Identify the blood parasite species.
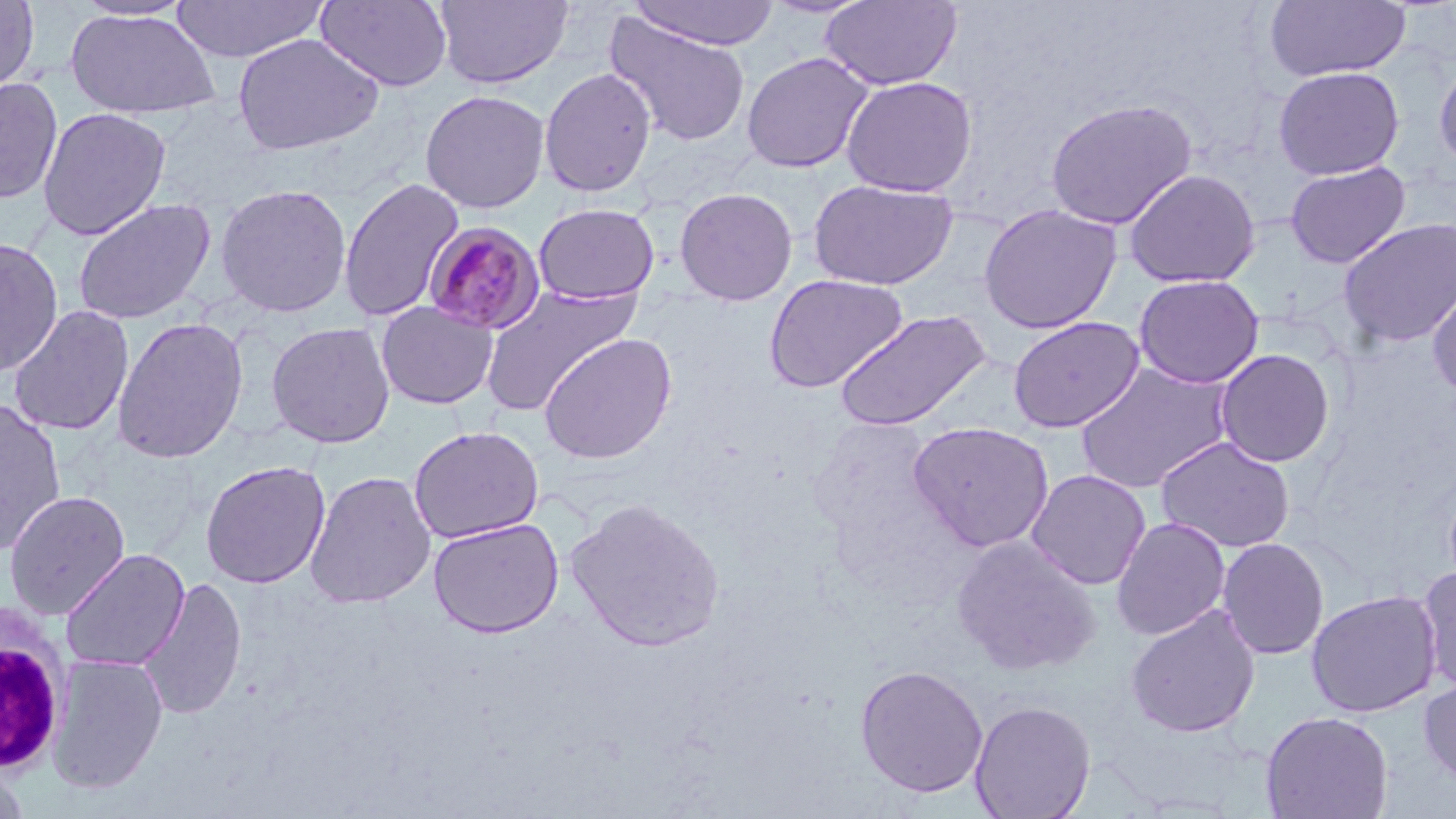
Plasmodium malariae.

Summary:
  - Coordinate format: approximate bounding boxes as (x1, y1, x2, y2) in pixels
  - Uninfected red blood cell locations: (0, 0, 39, 96), (71, 0, 197, 21), (315, 0, 453, 93), (433, 0, 574, 89), (627, 0, 780, 50), (821, 0, 963, 91), (168, 1, 331, 62), (1264, 1, 1411, 82), (64, 8, 220, 120), (603, 12, 753, 148), (232, 33, 384, 156), (741, 52, 874, 173), (1434, 56, 1456, 171), (1273, 66, 1404, 180), (539, 68, 657, 198), (841, 76, 977, 197), (0, 77, 62, 205), (420, 89, 550, 214), (1045, 98, 1197, 229), (37, 107, 171, 240), (1285, 161, 1411, 268), (1123, 169, 1260, 288), (339, 177, 464, 323), (807, 179, 959, 290), (215, 183, 352, 318), (674, 187, 798, 306), (73, 197, 216, 325), (533, 203, 660, 304), (979, 203, 1122, 334), (1338, 218, 1456, 348), (0, 238, 64, 377), (763, 273, 909, 393), (1134, 274, 1264, 389), (1427, 279, 1456, 400), (479, 285, 641, 417), (376, 300, 498, 409), (8, 305, 134, 436), (832, 309, 992, 431), (112, 316, 249, 463), (1008, 316, 1145, 433), (266, 321, 394, 448), (538, 332, 677, 465), (1214, 349, 1335, 468), (1074, 362, 1234, 495), (0, 398, 67, 557), (908, 421, 1055, 553), (408, 425, 544, 543), (1155, 436, 1295, 554), (200, 460, 330, 589), (1026, 469, 1151, 590), (304, 470, 436, 609), (3, 490, 131, 620), (564, 497, 726, 652), (1111, 516, 1231, 641), (428, 517, 564, 637), (952, 536, 1100, 675), (1217, 537, 1329, 660), (60, 549, 189, 671), (1417, 564, 1456, 695), (136, 576, 247, 720), (1306, 590, 1441, 718), (1125, 605, 1261, 738), (47, 654, 168, 794), (854, 664, 989, 798), (1419, 678, 1456, 789), (969, 699, 1097, 819), (1260, 710, 1393, 819), (0, 759, 32, 819)
  - White blood cell locations: (0, 607, 69, 773)
  - Plasmodium malariae-infected red blood cell locations: (422, 221, 546, 336)
  - Stain: May-Grünwald-Giemsa
  - Image size: 1456×819 pixels
  - Modality: optical microscopy
  - Preparation: thin blood smear
  - Field of view: single
  - Magnification: 1000x